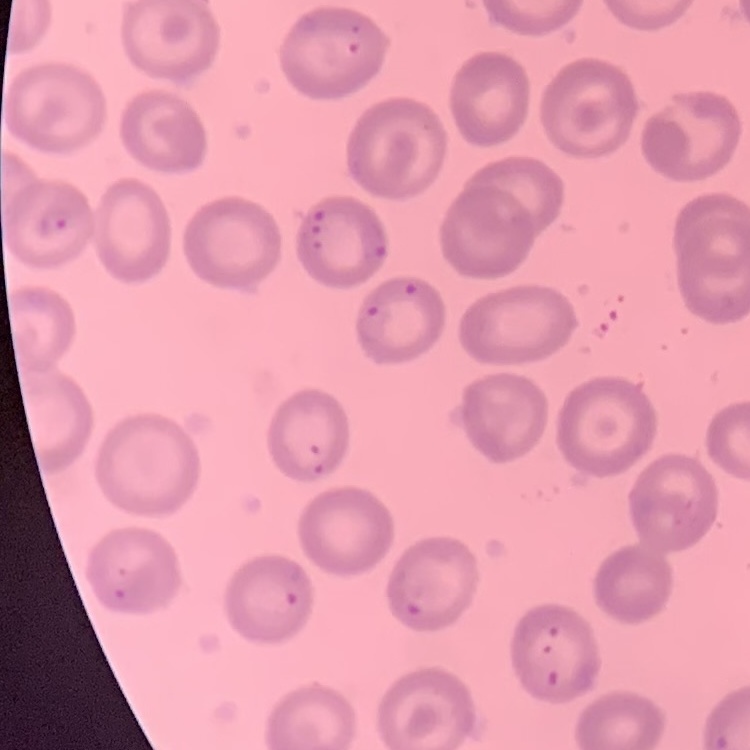
erythrocyte morphology = no rouleaux formation
stain = Field's or Giemsa
image type = one tile cut from a larger photomicrograph
preparation = thin blood film